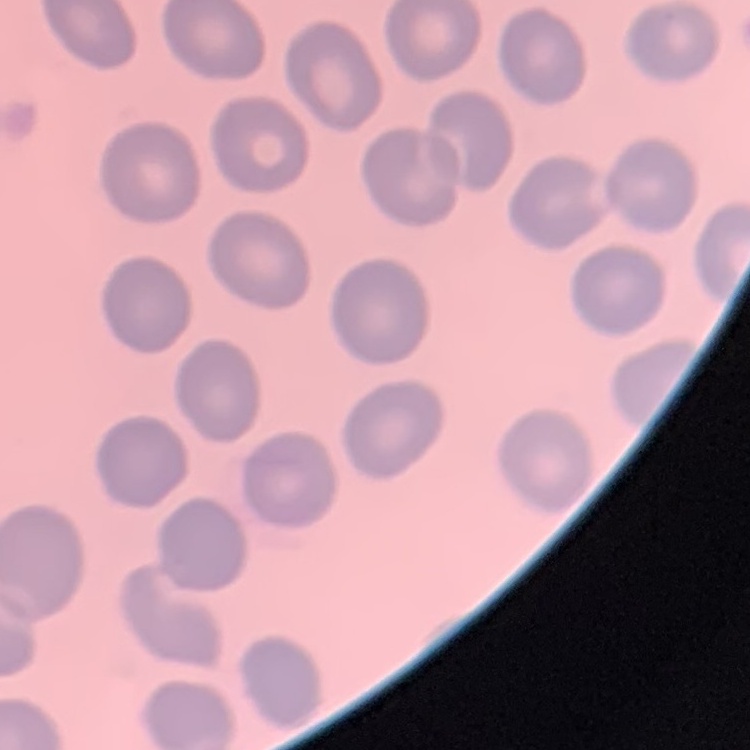 The erythrocytes exhibit no rouleaux formation. One tile cut from a larger photomicrograph. Stained with either Field's or Giemsa. Thin blood smear.